Identify the parasite.
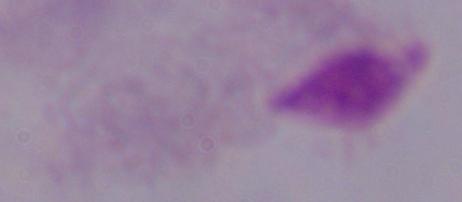
This is a trichomonad.

Photomicrograph. 1000x magnification.